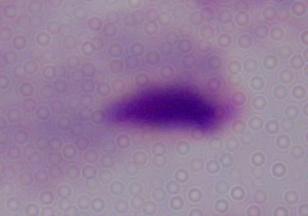
Summary:
  - Modality: photomicrograph
  - Identification: trichomonad
  - Magnification: 1000x